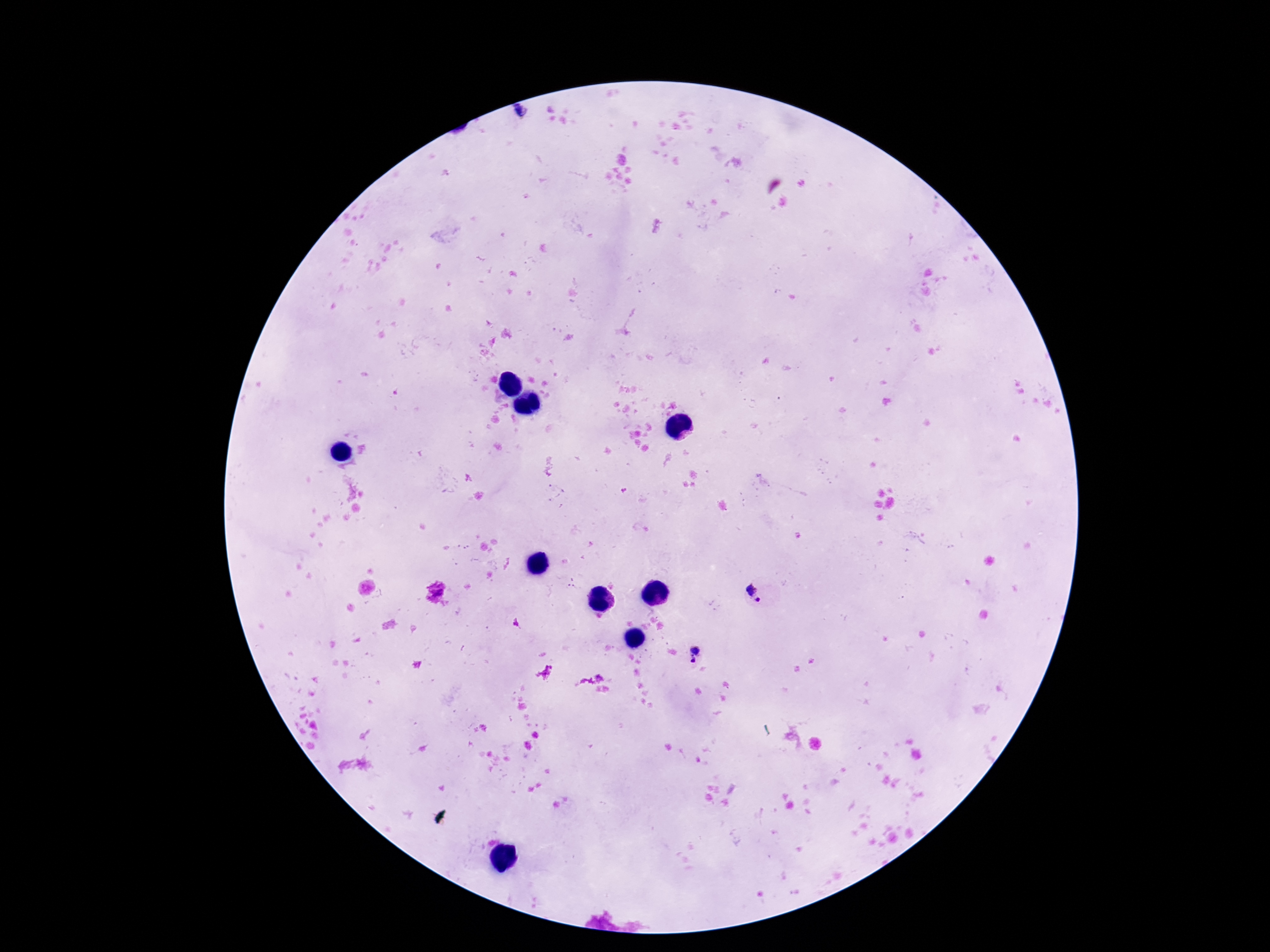 Approximate centers as [x, y] in pixels. Plasmodium parasite locations: [759, 592], [697, 654]. Image is 1270×952 pixels. 100x magnification. Patient malaria status: infected. Photographed through the microscope eyepiece with a smartphone camera. Giemsa-stained preparation. One field from this slide. Thick blood smear.